Assess this cell for malaria.
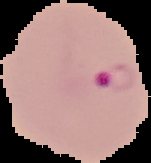

Parasitized.

{
  "image_type": "cell region segmented out of the field of view; surrounding area masked to black",
  "image_size": "151×163 pixels",
  "preparation": "thin blood smear"
}